Locate every Plasmodium parasite.
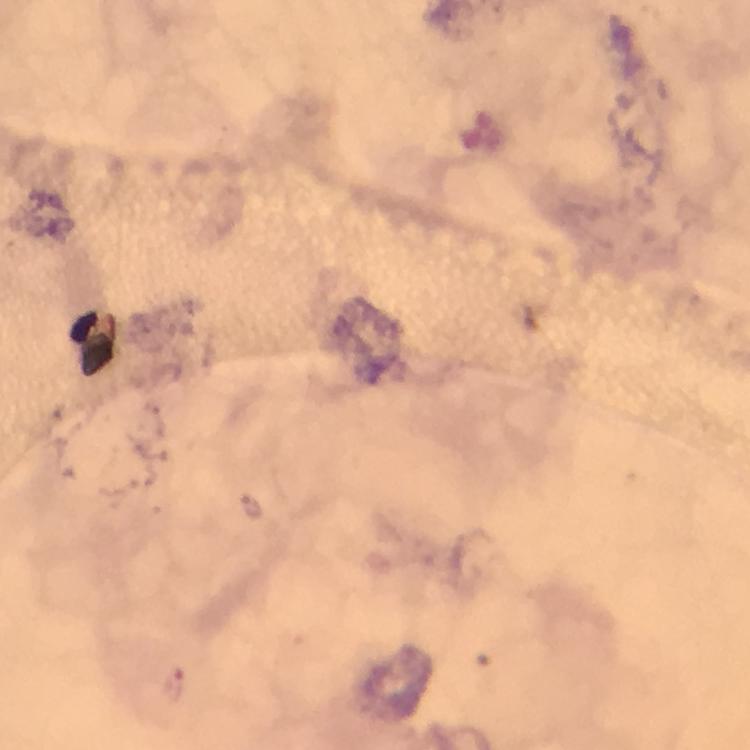

Approximate centers as {x, y} in pixels.
Plasmodium parasites: {252, 506}, {174, 687}.

cropped from = one field of view
image size = 750×750 pixels
stain = Giemsa
context = from a diagnostic examination for malaria
capture = smartphone mounted on the microscope
preparation = thick smear
immersion oil = applied
magnification = 100x